Point out each Plasmodium parasite.
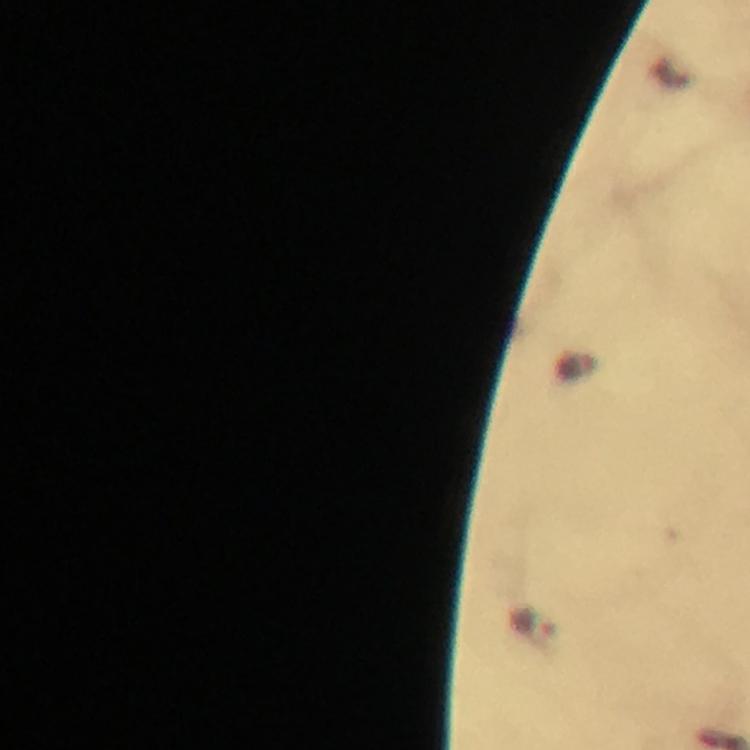

Approximate centers as (x, y) in pixels.
Plasmodium parasites: (533, 623).

Giemsa-stained preparation. 100x magnification. Thick smear. Image is 750×750 pixels. From a diagnostic examination for malaria. Cropped region of a single field of view. Immersion oil applied. Photographed with a smartphone mounted on the microscope.